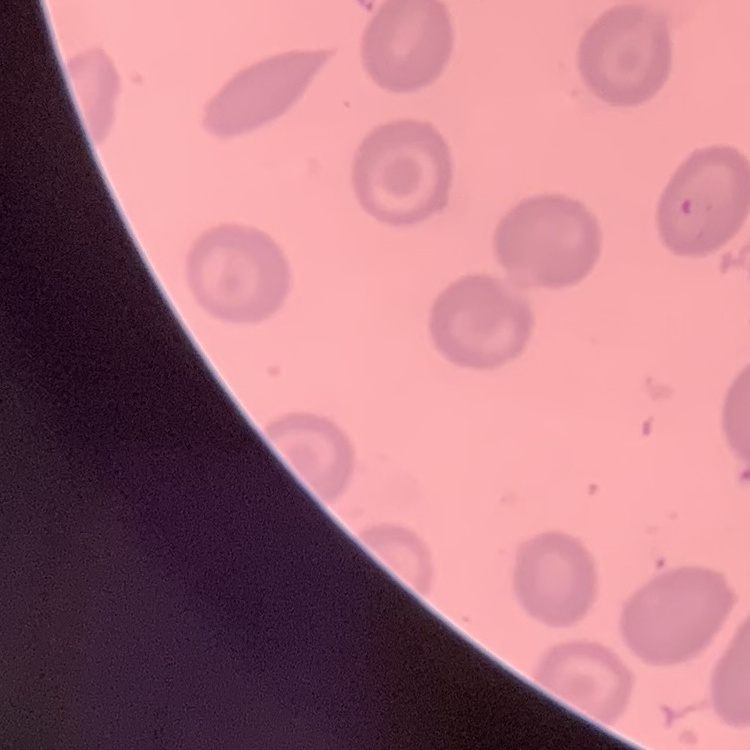

erythrocyte morphology = no rouleaux formation
stain = Field's or Giemsa
image type = square crop of a larger photomicrograph
preparation = thin peripheral smear